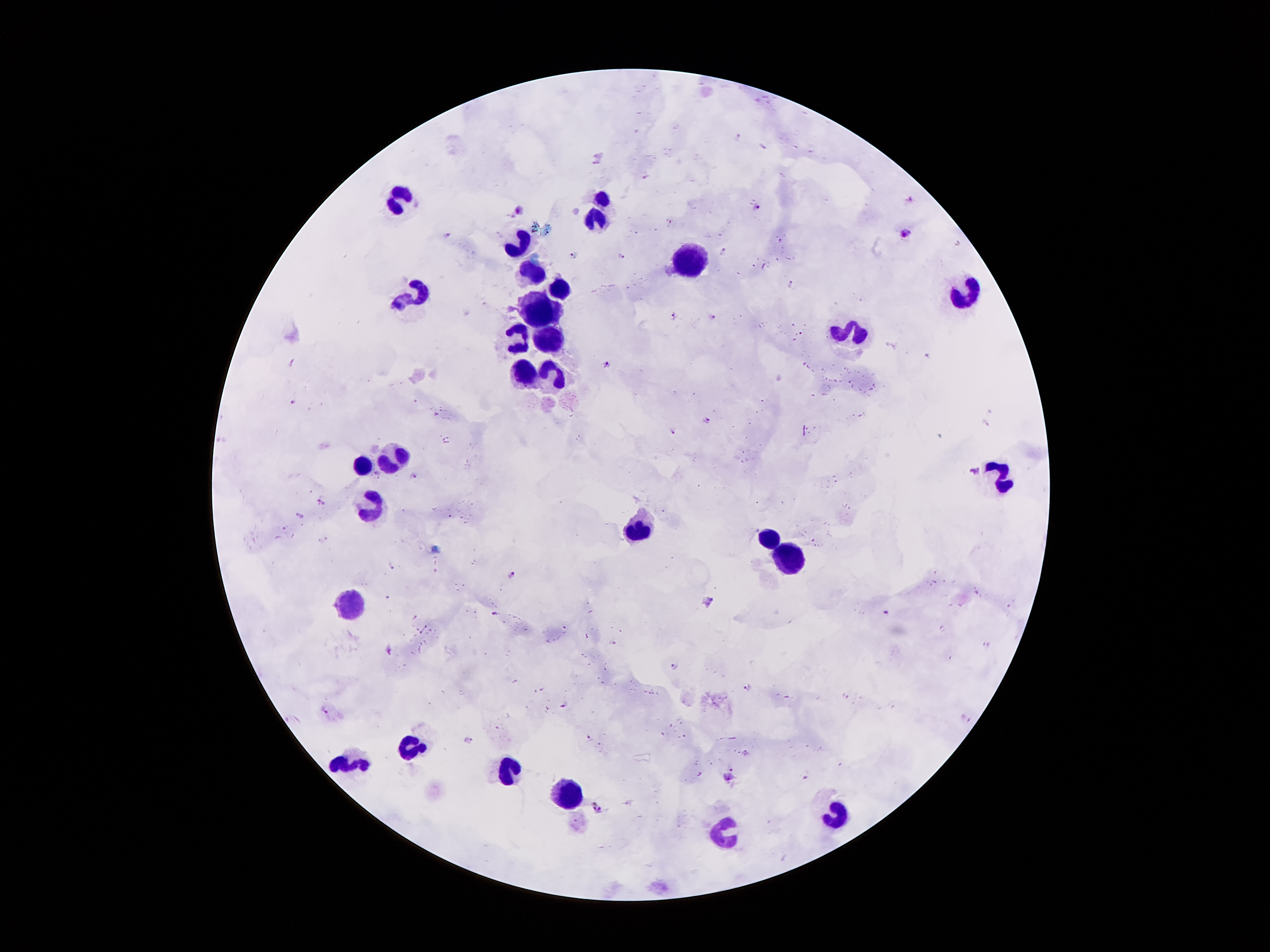

{
  "magnification": "100x",
  "leukocyte_locations": "approximate centers as {x, y} in pixels: {399, 196}, {603, 196}, {595, 219}, {523, 238}, {691, 263}, {528, 270}, {560, 288}, {967, 292}, {419, 293}, {542, 311}, {855, 330}, {548, 336}, {518, 337}, {524, 375}, {552, 376}, {390, 459}, {364, 465}, {1007, 480}, {372, 504}, {639, 528}, {770, 539}, {788, 560}, {352, 604}, {414, 744}, {351, 761}, {510, 772}, {571, 792}, {840, 817}, {728, 833}",
  "plasmodium_parasite_locations": "approximate centers as {x, y} in pixels: {647, 174}, {912, 200}, {758, 207}, {521, 209}, {670, 223}, {904, 231}, {445, 234}, {621, 256}, {791, 285}, {673, 316}, {711, 317}, {929, 354}, {609, 362}, {292, 363}, {295, 400}, {707, 420}, {674, 431}, {975, 472}, {412, 474}, {323, 502}, {303, 513}, {513, 577}, {708, 601}, {885, 611}, {495, 613}, {388, 648}, {673, 664}, {750, 685}, {563, 704}, {324, 709}, {967, 718}, {588, 737}, {468, 740}, {727, 778}, {804, 778}, {597, 808}",
  "preparation": "thick blood film",
  "field_of_view": "one from this slide",
  "patient_malaria_status": "infected with Plasmodium falciparum",
  "stain": "Giemsa",
  "capture": "smartphone through the microscope eyepiece",
  "image_size": "1270×952 pixels"
}